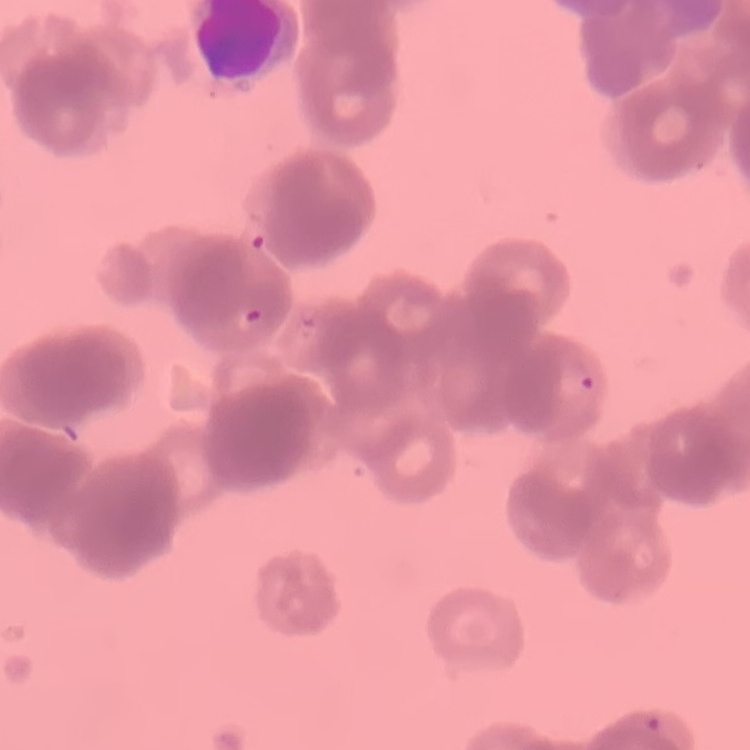
The erythrocytes show rouleaux formation. Thin blood smear. Stained with either Field's or Giemsa. One tile cut from a larger photomicrograph.